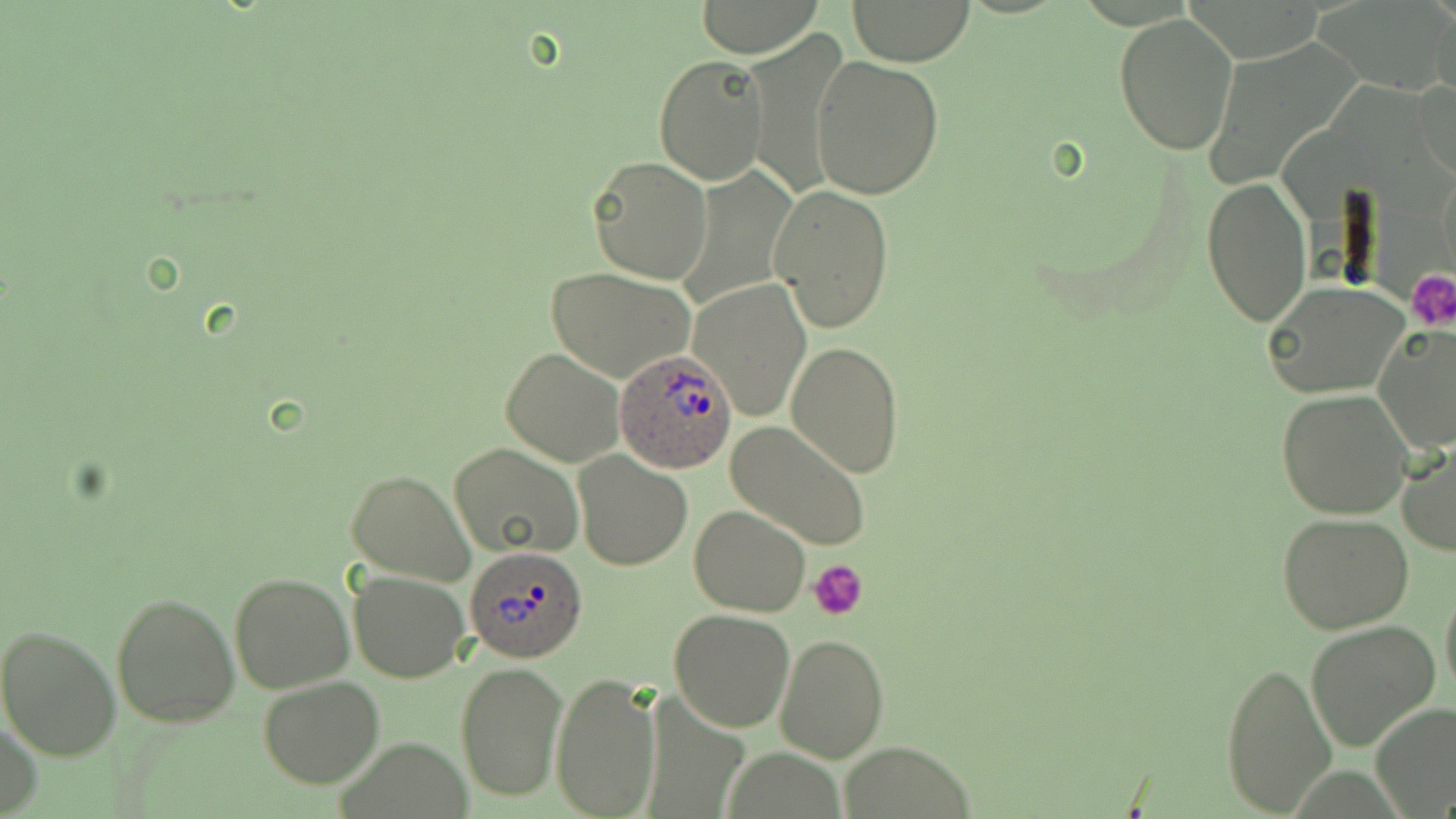
slide_level_diagnosis: Plasmodium ovale
uninfected_red_blood_cell_locations: 'approximate bounding boxes as (x1,y1)-(x2,y2) corner pairs in pixels: (692,1)-(823,56), (845,1)-(978,64), (1432,3)-(1456,102), (1113,14)-(1240,157), (740,30)-(847,200), (654,55)-(768,185), (812,55)-(944,200), (1414,76)-(1456,184), (587,156)-(712,284), (676,166)-(799,314), (1201,177)-(1314,328), (769,184)-(894,333), (547,266)-(696,383), (690,279)-(809,419), (1264,282)-(1409,400), (1374,324)-(1456,455), (786,339)-(904,478), (500,348)-(624,467), (1276,389)-(1415,521), (725,421)-(872,552), (1398,442)-(1456,558), (450,444)-(585,563), (573,451)-(691,570), (345,468)-(476,584), (689,505)-(812,616), (1275,512)-(1415,634), (228,570)-(354,696), (348,571)-(470,682), (1439,575)-(1456,708), (110,589)-(241,730), (2,608)-(239,744), (669,608)-(797,733), (1305,620)-(1442,754), (0,623)-(121,762), (773,631)-(890,762), (454,659)-(568,803), (1219,659)-(1338,818), (551,669)-(660,819), (257,676)-(383,788), (1371,703)-(1456,816), (0,716)-(42,819), (840,745)-(976,818)'
modality: light microscopy
field_of_view: single
plasmodium_ovale_infected_red_blood_cell_locations: 'approximate bounding boxes as (x1,y1)-(x2,y2) corner pairs in pixels: (614,349)-(736,472), (465,545)-(588,665)'
stain: May-Grünwald-Giemsa
platelet_locations: 'approximate bounding boxes as (x1,y1)-(x2,y2) corner pairs in pixels: (1408,270)-(1456,329), (809,560)-(868,621)'
magnification: 1000x
preparation: thin blood film
image_size: 1456×819 pixels